Point out malaria parasites and leukocytes.
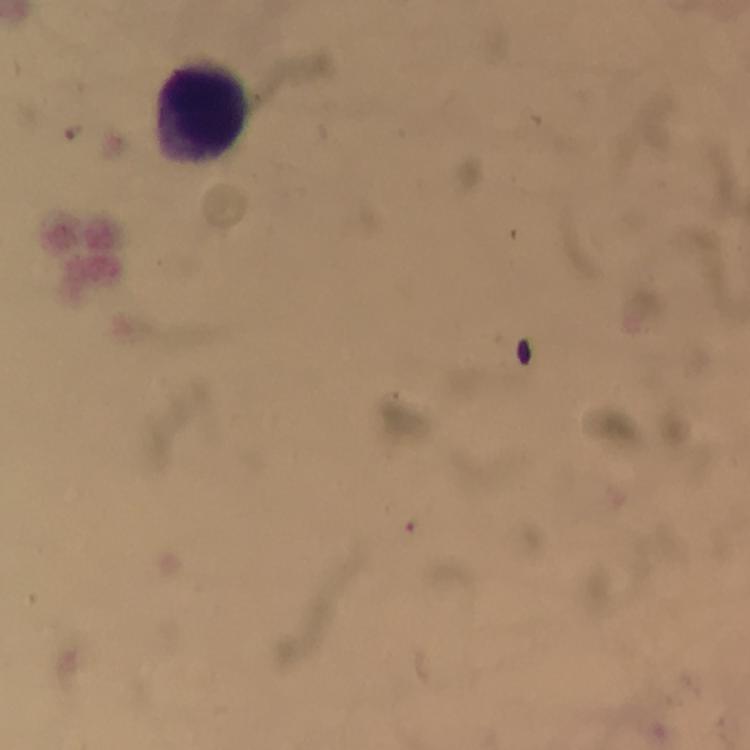
No malaria parasites seen.
Approximate centers as [x, y] in pixels.
Leukocytes: [202, 111].

From a malaria diagnostic workup. Giemsa-stained preparation. Smartphone photograph taken through a microscope. Image is 750×750 pixels. A crop from one field of view. Thick blood smear. At 100x magnification. Immersion oil applied.